State which parasite is depicted.
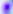

Toxoplasma gondii.

Micrograph. Captured at 400x magnification.